Identify the blood parasite species.
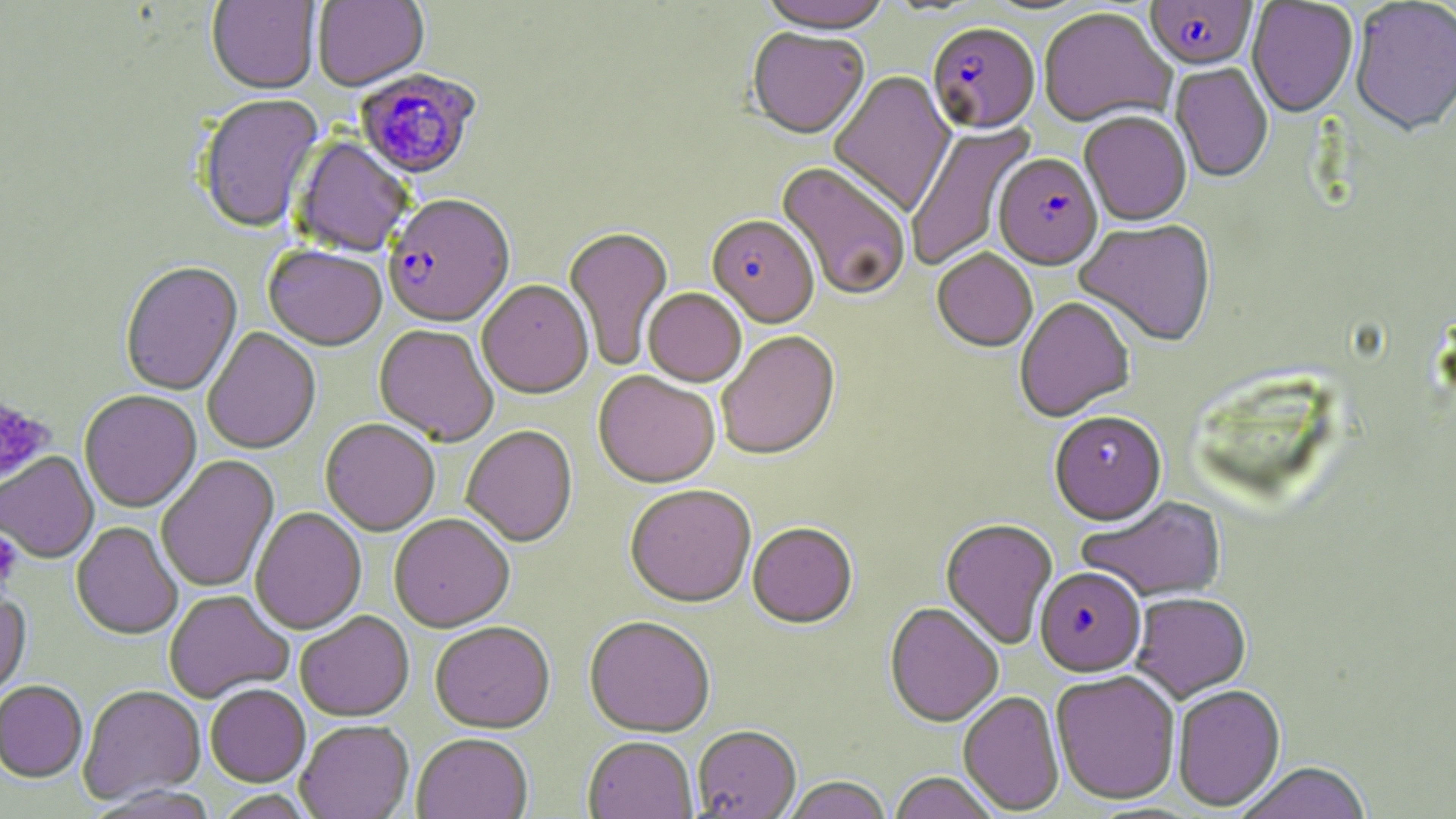
Plasmodium falciparum.

image size = 1456×819 pixels
uninfected red blood cell locations = approximate bounding boxes as (x1,y1)-(x2,y2) corner pairs in pixels: (313,0)-(429,92), (757,0)-(892,38), (1350,0)-(1456,140), (206,1)-(320,97), (1247,1)-(1359,120), (1039,9)-(1176,130), (747,29)-(869,142), (1170,63)-(1273,184), (828,71)-(956,217), (197,96)-(325,235), (1079,113)-(1192,228), (905,121)-(1037,272), (292,137)-(413,258), (774,164)-(911,301), (1074,221)-(1216,348), (563,228)-(674,371), (263,247)-(387,352), (932,251)-(1037,354), (120,263)-(243,397), (477,281)-(593,401), (643,290)-(746,388), (1015,298)-(1135,424), (374,325)-(499,447), (203,328)-(321,456), (716,332)-(840,462), (593,372)-(719,491), (79,391)-(201,514), (1049,413)-(1167,527), (320,419)-(440,536), (461,426)-(578,549), (0,452)-(98,564), (156,456)-(280,593), (624,487)-(756,611), (1076,497)-(1227,603), (250,508)-(366,635), (389,516)-(515,633), (940,519)-(1058,651), (71,523)-(183,641), (748,525)-(858,631), (0,588)-(31,702), (164,591)-(294,704), (1131,593)-(1251,702), (884,604)-(1004,729), (295,612)-(414,723), (584,618)-(716,738), (430,624)-(555,734), (1050,671)-(1181,805), (0,682)-(88,783), (206,685)-(310,787), (1172,685)-(1286,813), (78,686)-(205,805), (958,691)-(1065,815), (295,722)-(413,819), (691,727)-(801,818), (412,735)-(533,819), (583,738)-(698,819), (1234,762)-(1373,819), (888,772)-(1001,819), (782,777)-(893,819)
field of view = one of a larger specimen
modality = optical microscopy
magnification = 1000x
platelet locations = approximate bounding boxes as (x1,y1)-(x2,y2) corner pairs in pixels: (0,394)-(56,488), (0,532)-(22,587)
preparation = thin blood film
stain = May-Grünwald-Giemsa
Plasmodium falciparum-infected red blood cell locations = approximate bounding boxes as (x1,y1)-(x2,y2) corner pairs in pixels: (1145,1)-(1258,73), (927,25)-(1041,138), (354,70)-(480,181), (993,155)-(1103,273), (383,196)-(515,330), (706,217)-(819,330), (1034,568)-(1146,677)